Locate every malaria parasite.
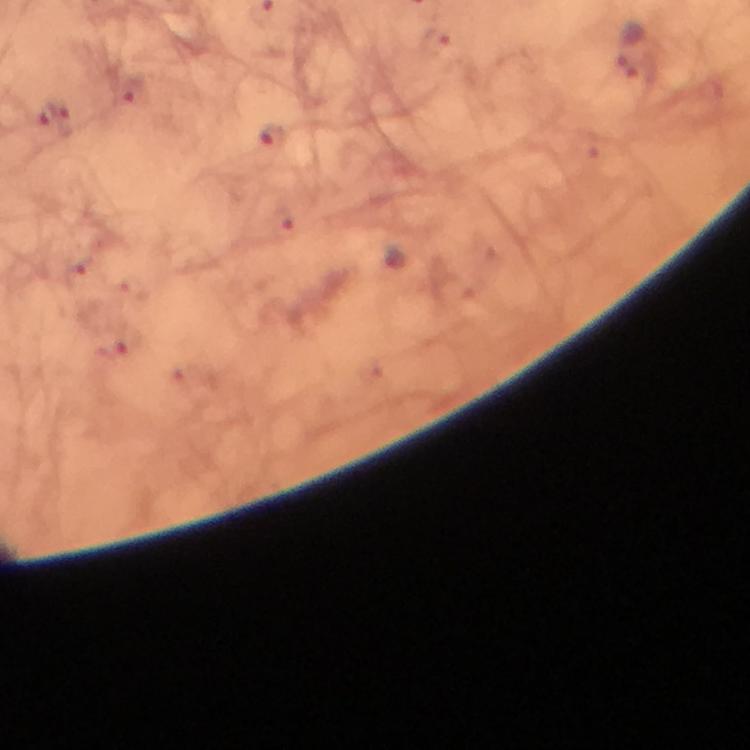

Approximate centers as [x, y] in pixels.
Malaria parasites: [628, 46], [57, 120], [272, 138].

A crop from one field of view. Giemsa-stained preparation. Thick blood film. Immersion oil was used. Photographed through the microscope with a smartphone camera. From a malaria diagnostic workup. 100x magnification. Image is 750×750 pixels.